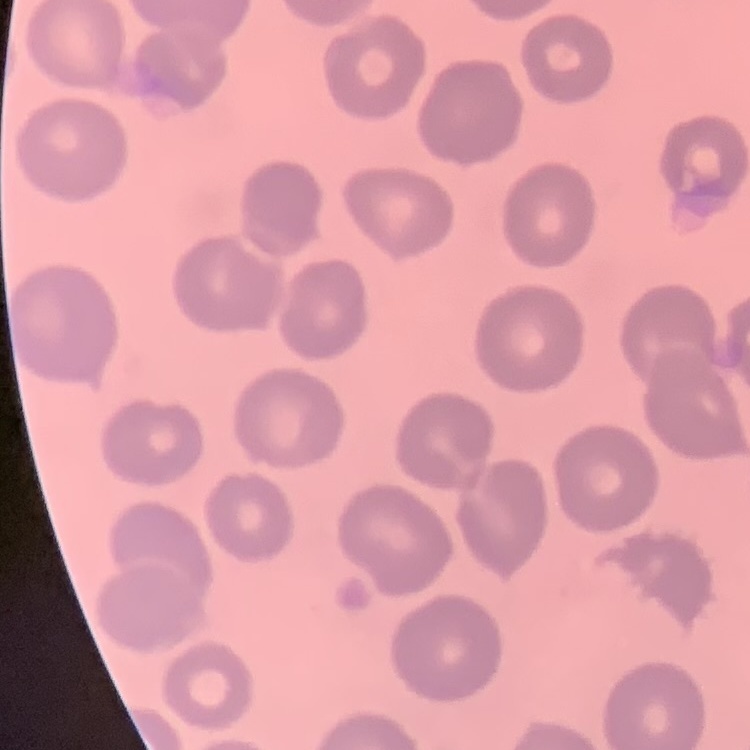

{
  "red_blood_cell_morphology": "no rouleaux formation",
  "preparation": "thin blood smear",
  "stain": "Field's or Giemsa",
  "image_type": "square crop of a larger photomicrograph"
}